Report the malaria status.
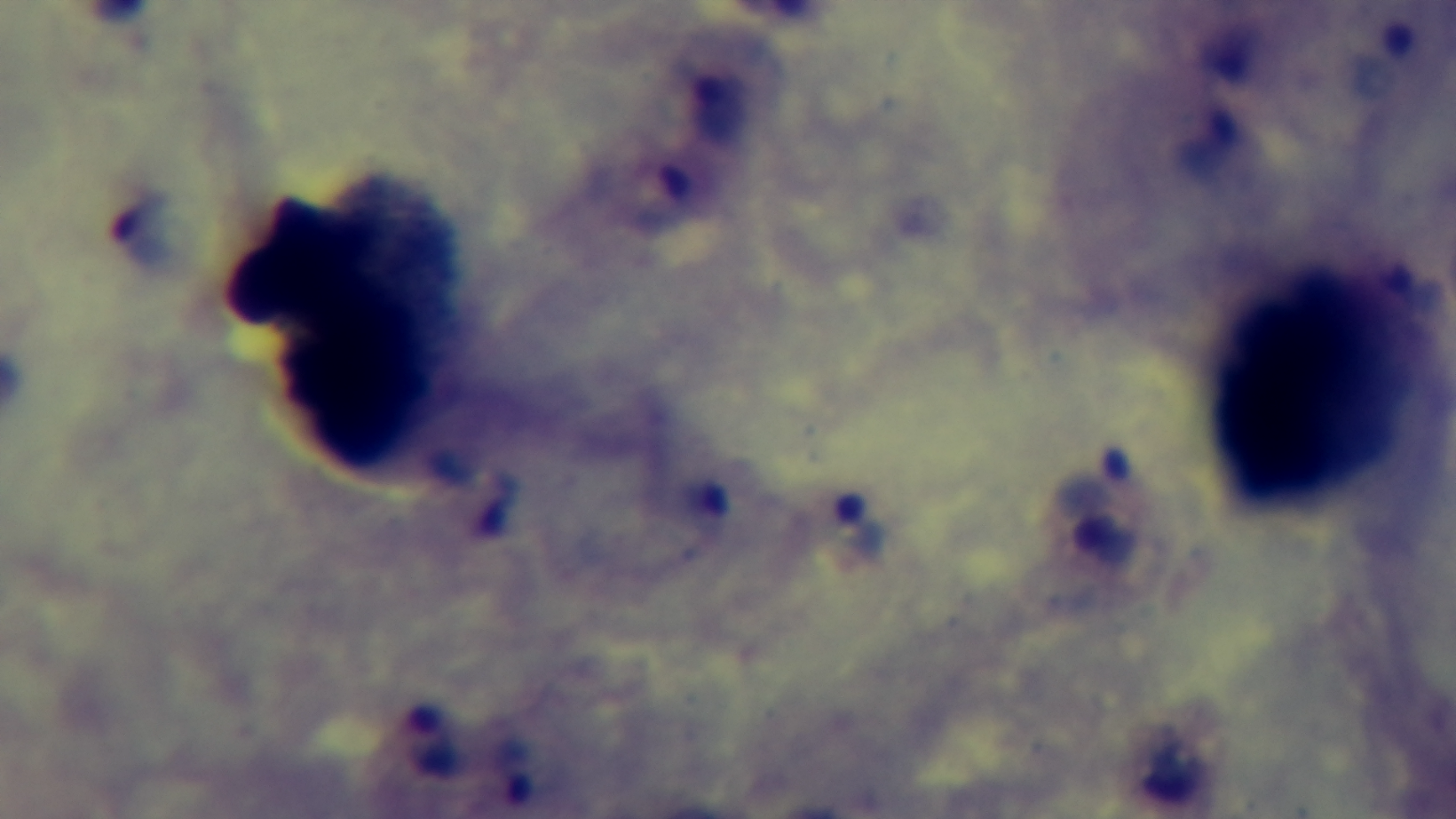

It is infected.

Photomicrograph. Giemsa stain. One field from the slide. 100x oil-immersion objective. Mounted 4K digital camera. Preparation: thick.